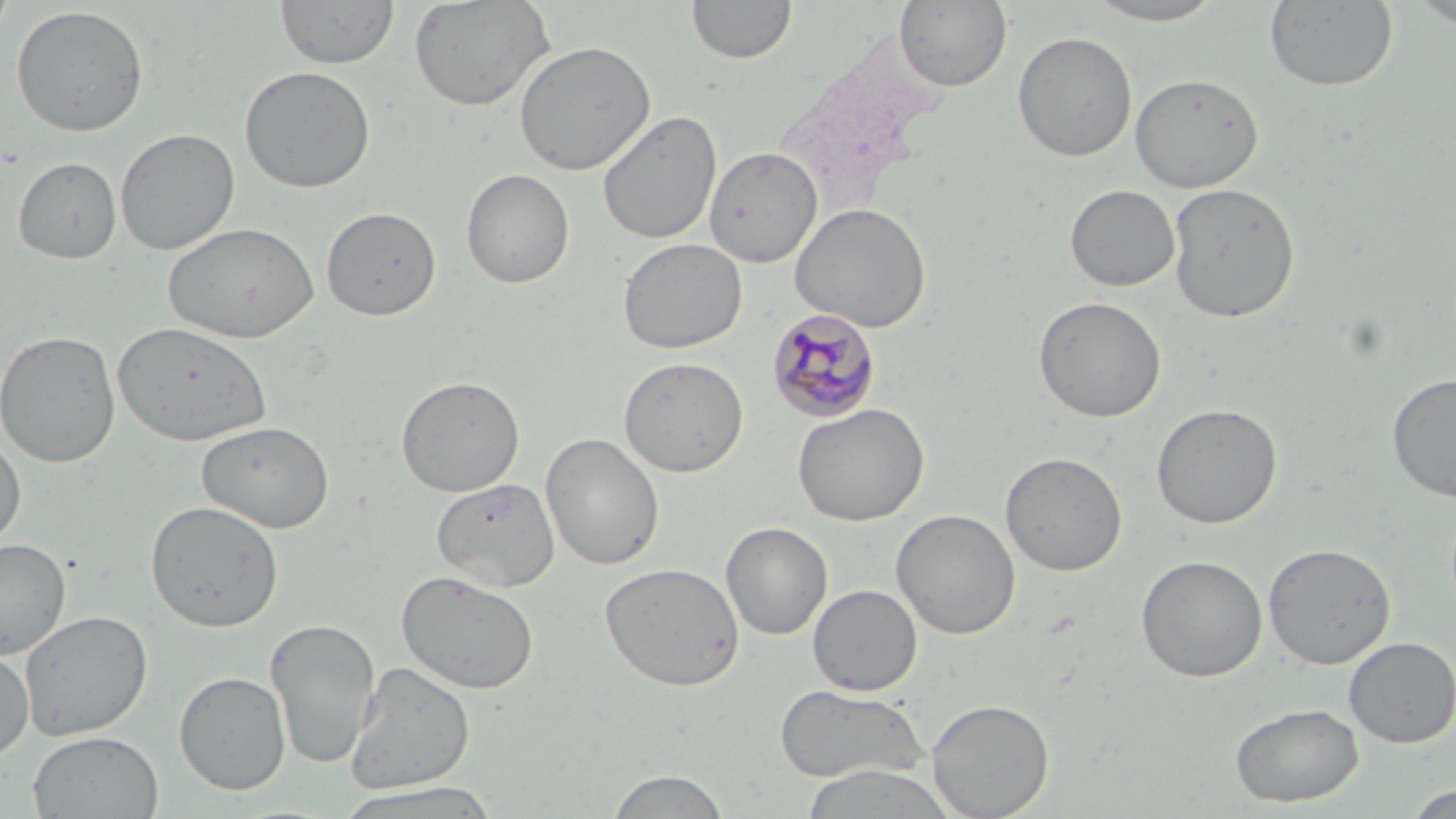

Summary:
  - Coordinate format: approximate bounding boxes as (x1,y1)-(x2,y2) corner pairs in pixels
  - Uninfected red blood cell locations: (0,0)-(17,49), (275,0)-(400,70), (408,0)-(555,112), (893,0)-(1013,92), (1080,0)-(1231,26), (687,1)-(797,65), (1263,1)-(1398,92), (1407,1)-(1456,29), (11,5)-(149,137), (1012,30)-(1138,162), (513,39)-(657,175), (239,65)-(376,193), (1130,73)-(1263,192), (598,109)-(723,245), (115,128)-(239,255), (704,146)-(823,268), (13,156)-(121,263), (461,168)-(575,289), (1167,182)-(1300,323), (1065,184)-(1181,292), (790,202)-(932,332), (322,206)-(441,320), (163,222)-(319,344), (617,238)-(747,354), (1032,295)-(1167,422), (111,320)-(271,447), (0,329)-(121,468), (618,356)-(749,477), (1386,371)-(1456,503), (395,374)-(526,497), (792,402)-(930,526), (1150,403)-(1283,529), (196,420)-(335,532), (541,432)-(665,571), (0,433)-(26,551), (1000,451)-(1127,576), (432,477)-(559,593), (145,500)-(283,632), (891,508)-(1021,639), (721,521)-(833,640), (0,538)-(71,659), (1262,542)-(1396,669), (1135,554)-(1268,682), (599,561)-(745,690), (396,569)-(539,694), (807,584)-(922,696), (19,610)-(152,742), (264,618)-(381,769), (1343,636)-(1456,747), (0,647)-(34,760), (345,662)-(476,795), (174,670)-(291,795), (774,683)-(930,785), (926,699)-(1055,818), (1230,702)-(1363,807), (28,730)-(164,819), (800,764)-(957,819), (605,768)-(732,818), (333,782)-(503,818), (1401,782)-(1455,817)
  - Plasmodium malariae-infected red blood cell locations: (766,307)-(882,423)
  - Slide-level diagnosis: Plasmodium malariae
  - Stain: May-Grünwald-Giemsa
  - Image size: 1456×819 pixels
  - Field of view: one of a larger specimen
  - Magnification: 1000x
  - Preparation: thin blood film
  - Modality: light microscopy